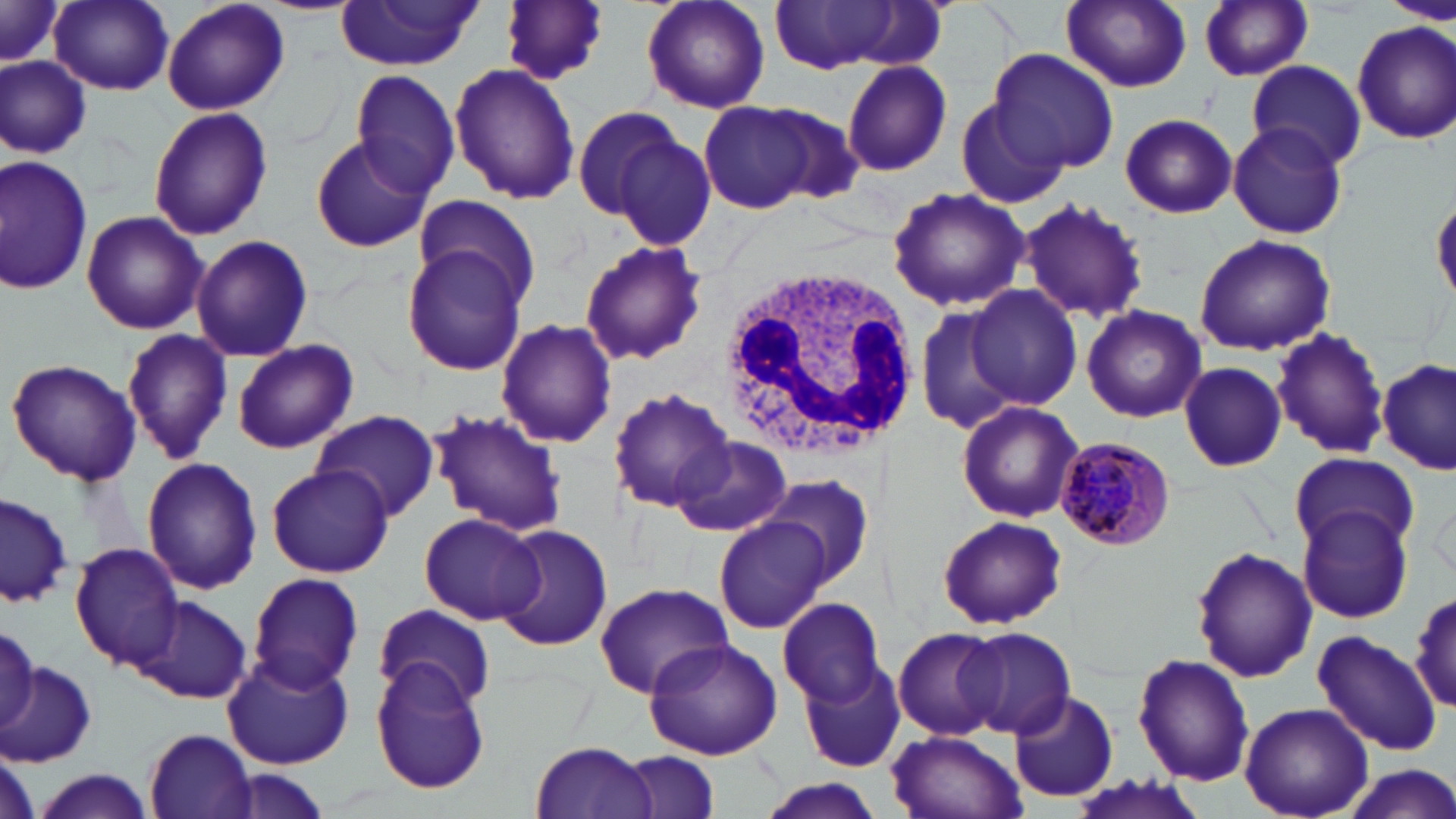

slide-level diagnosis = Plasmodium malariae
magnification = 1000x
field of view = single
Plasmodium malariae-infected red blood cell locations = approximate bounding boxes as (x1, y1, x2, y2) in pixels: (1054, 437, 1175, 551)
white blood cell locations = approximate bounding boxes as (x1, y1, x2, y2) in pixels: (718, 262, 914, 457)
preparation = thin blood smear
image size = 1456×819 pixels
stain = May-Grünwald-Giemsa
modality = optical microscopy
uninfected red blood cell locations = approximate bounding boxes as (x1, y1, x2, y2) in pixels: (0, 0, 66, 68), (160, 0, 290, 116), (499, 0, 611, 85), (637, 0, 773, 115), (1059, 0, 1194, 95), (1382, 0, 1452, 25), (333, 1, 485, 72), (50, 2, 176, 95), (773, 2, 910, 74), (1198, 2, 1315, 82), (1353, 22, 1456, 143), (987, 48, 1121, 174), (1, 55, 92, 159), (1246, 59, 1367, 170), (841, 60, 952, 177), (449, 63, 581, 204), (350, 70, 463, 196), (950, 97, 1066, 205), (698, 99, 818, 214), (571, 104, 685, 220), (148, 105, 273, 241), (753, 105, 868, 205), (1118, 113, 1237, 218), (1226, 121, 1350, 240), (612, 131, 718, 255), (308, 134, 434, 253), (0, 156, 92, 296), (885, 188, 1029, 313), (413, 192, 542, 311), (1018, 199, 1149, 323), (80, 209, 206, 334), (1193, 232, 1336, 357), (190, 235, 313, 361), (578, 239, 708, 369), (402, 245, 528, 377), (965, 284, 1084, 410), (914, 301, 1027, 435), (1081, 305, 1206, 423), (494, 318, 619, 448), (119, 326, 232, 466), (1272, 326, 1391, 461), (231, 338, 359, 454), (6, 357, 143, 486), (1379, 359, 1453, 477), (1176, 360, 1286, 471), (608, 385, 737, 515), (955, 398, 1082, 523), (427, 407, 570, 536), (312, 410, 441, 521), (671, 434, 793, 538), (1289, 450, 1417, 556), (140, 457, 262, 596), (265, 463, 393, 577), (756, 471, 876, 588), (0, 491, 74, 610), (1296, 502, 1415, 623), (419, 512, 546, 624), (937, 514, 1066, 631), (716, 516, 834, 634), (495, 526, 614, 652), (69, 543, 186, 667), (1190, 546, 1317, 686), (245, 572, 364, 693), (594, 580, 733, 700), (1410, 587, 1456, 715), (134, 597, 253, 704), (776, 597, 884, 706), (374, 605, 495, 710), (0, 622, 38, 732), (904, 623, 1058, 783), (892, 627, 1006, 742), (958, 627, 1075, 738), (1313, 631, 1442, 755), (641, 638, 783, 759), (1132, 652, 1251, 786), (223, 653, 355, 769), (370, 656, 492, 794), (799, 657, 906, 775), (0, 660, 97, 766), (1009, 691, 1119, 803), (1239, 702, 1372, 818), (143, 730, 260, 818), (885, 730, 1027, 819), (530, 740, 660, 819), (619, 752, 722, 819), (1338, 765, 1456, 819), (24, 770, 159, 819), (1069, 772, 1210, 819), (753, 779, 888, 819)